Point out each Plasmodium parasite.
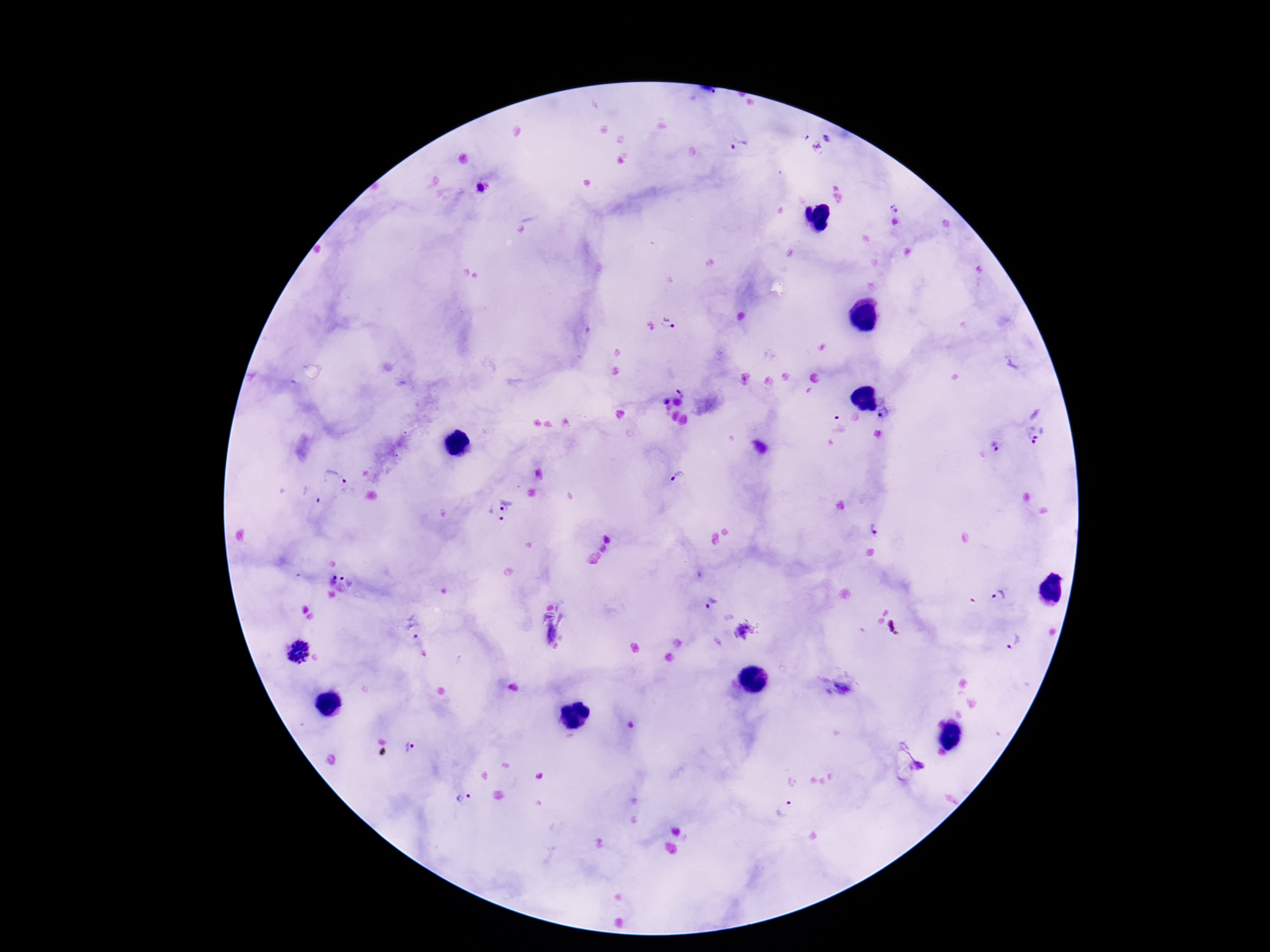

Approximate centers as (x, y) in pixels.
Plasmodium parasites: (827, 139), (816, 147), (740, 148), (894, 208), (667, 323), (682, 392), (885, 415), (835, 423), (1031, 435), (995, 446), (334, 479), (679, 479), (312, 498), (498, 509), (874, 530), (348, 577), (1001, 596), (710, 603), (412, 626), (741, 632), (1011, 640), (297, 651), (412, 749), (923, 765), (465, 798), (785, 809).

Patient malaria status: positive. Thick blood smear. Giemsa stain. One field from this slide. Image is 1270×952 pixels. 100x magnification. Photographed through the microscope eyepiece with a smartphone camera.